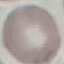
malaria status = uninfected
stain = Giemsa
capture = smartphone through the microscope eyepiece
image type = automatically extracted cell patch, resized to 64 × 64 pixels
preparation = thin blood smear